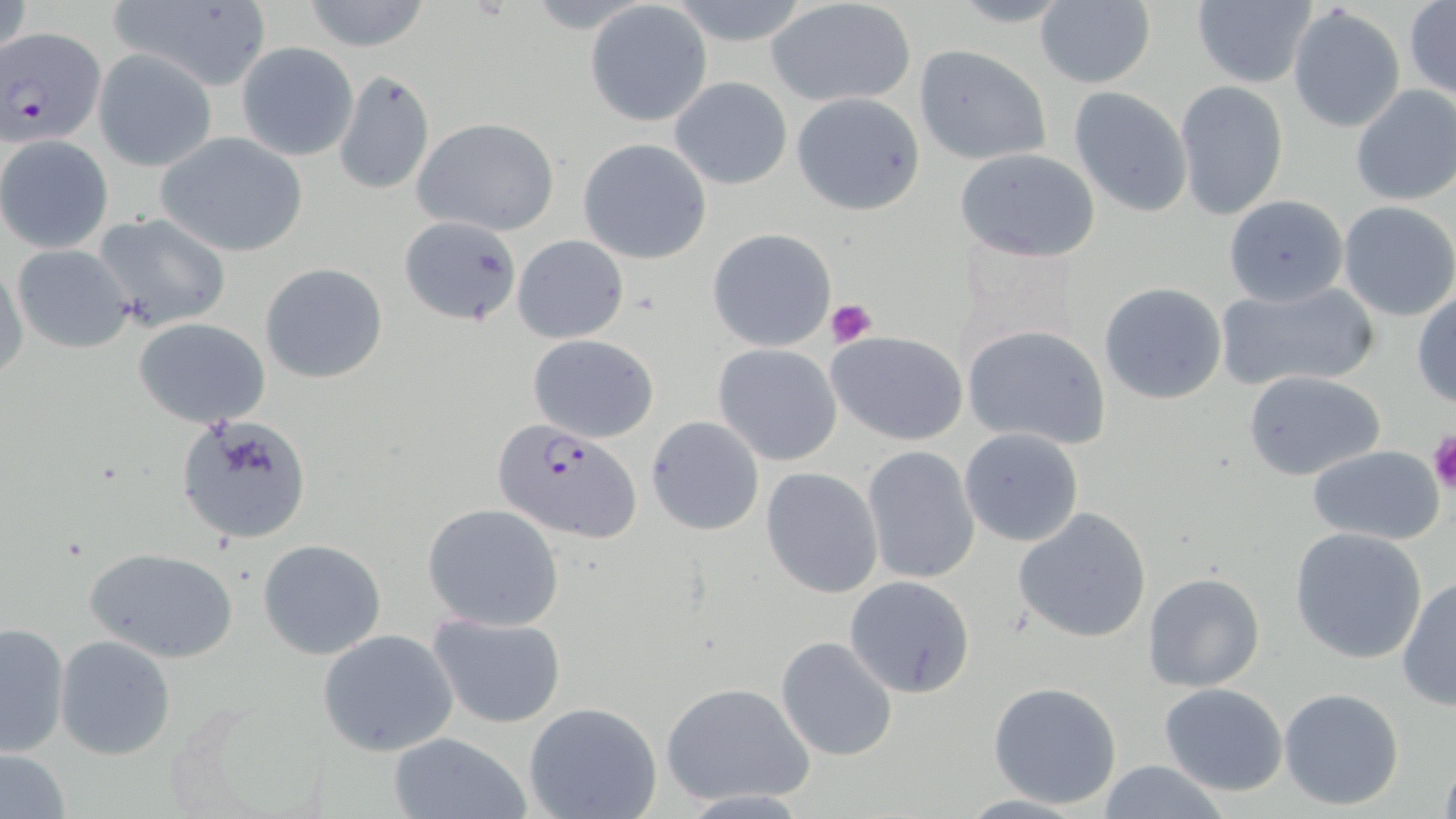
slide-level diagnosis = Plasmodium falciparum
modality = light microscopy
Plasmodium falciparum-infected red blood cell locations = approximate bounding boxes as named x1/y1/x2/y2 corners in pixels: (x1=1, y1=28, x2=106, y2=149), (x1=492, y1=420, x2=642, y2=544)
preparation = thin blood smear
magnification = 1000x
uninfected red blood cell locations = approximate bounding boxes as named x1/y1/x2/y2 corners in pixels: (x1=300, y1=0, x2=431, y2=52), (x1=662, y1=0, x2=819, y2=49), (x1=943, y1=0, x2=1081, y2=28), (x1=1034, y1=0, x2=1157, y2=89), (x1=107, y1=1, x2=273, y2=91), (x1=765, y1=1, x2=917, y2=107), (x1=1190, y1=1, x2=1317, y2=88), (x1=585, y1=2, x2=712, y2=125), (x1=1404, y1=2, x2=1455, y2=101), (x1=1287, y1=4, x2=1406, y2=133), (x1=236, y1=42, x2=358, y2=161), (x1=914, y1=45, x2=1052, y2=166), (x1=93, y1=49, x2=216, y2=171), (x1=332, y1=69, x2=435, y2=196), (x1=669, y1=76, x2=793, y2=190), (x1=1174, y1=80, x2=1288, y2=222), (x1=1350, y1=84, x2=1456, y2=206), (x1=1068, y1=86, x2=1194, y2=217), (x1=791, y1=93, x2=925, y2=214), (x1=411, y1=116, x2=559, y2=236), (x1=155, y1=131, x2=309, y2=257), (x1=0, y1=135, x2=113, y2=253), (x1=577, y1=139, x2=712, y2=264), (x1=953, y1=147, x2=1101, y2=263), (x1=1223, y1=195, x2=1348, y2=306), (x1=1337, y1=202, x2=1456, y2=321), (x1=93, y1=212, x2=231, y2=331), (x1=401, y1=215, x2=521, y2=324), (x1=707, y1=228, x2=836, y2=351), (x1=512, y1=234, x2=629, y2=344), (x1=13, y1=244, x2=136, y2=352), (x1=1, y1=258, x2=26, y2=380), (x1=260, y1=262, x2=388, y2=384), (x1=1216, y1=280, x2=1382, y2=394), (x1=1098, y1=281, x2=1228, y2=405), (x1=1412, y1=289, x2=1456, y2=408), (x1=134, y1=317, x2=270, y2=428), (x1=961, y1=325, x2=1112, y2=450), (x1=826, y1=330, x2=968, y2=445), (x1=527, y1=334, x2=660, y2=441), (x1=712, y1=343, x2=843, y2=465), (x1=1243, y1=370, x2=1386, y2=481), (x1=176, y1=414, x2=314, y2=545), (x1=646, y1=416, x2=764, y2=535), (x1=959, y1=428, x2=1085, y2=547), (x1=1307, y1=445, x2=1447, y2=545), (x1=862, y1=446, x2=979, y2=584), (x1=760, y1=468, x2=884, y2=598), (x1=423, y1=503, x2=565, y2=631), (x1=1014, y1=508, x2=1153, y2=644), (x1=1288, y1=527, x2=1429, y2=664), (x1=257, y1=539, x2=387, y2=659), (x1=83, y1=546, x2=240, y2=663), (x1=1142, y1=571, x2=1267, y2=693), (x1=1396, y1=575, x2=1455, y2=709), (x1=844, y1=577, x2=974, y2=696), (x1=427, y1=613, x2=568, y2=727), (x1=0, y1=621, x2=70, y2=756), (x1=317, y1=628, x2=459, y2=756), (x1=55, y1=635, x2=176, y2=759), (x1=776, y1=635, x2=899, y2=762), (x1=661, y1=681, x2=815, y2=808), (x1=988, y1=681, x2=1123, y2=809), (x1=1159, y1=682, x2=1288, y2=796), (x1=1278, y1=688, x2=1404, y2=811), (x1=523, y1=701, x2=662, y2=819), (x1=387, y1=731, x2=530, y2=818), (x1=1, y1=750, x2=70, y2=818), (x1=1438, y1=753, x2=1456, y2=819), (x1=1095, y1=759, x2=1230, y2=819)
field of view = single
platelet locations = approximate bounding boxes as named x1/y1/x2/y2 corners in pixels: (x1=827, y1=299, x2=878, y2=347), (x1=1426, y1=429, x2=1456, y2=494)
stain = May-Grünwald-Giemsa
image size = 1456×819 pixels